Classify this cell by malaria status.
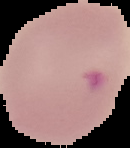
Parasitized.

image_type: cell region segmented out of the field of view; surrounding area masked to black
preparation: thin blood film
image_size: 130×148 pixels